Classify this cell by malaria status.
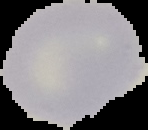
It is uninfected.

Summary:
  - Image type: cell region segmented out of the field of view; surrounding area masked to black
  - Preparation: thin blood film
  - Image size: 148×130 pixels